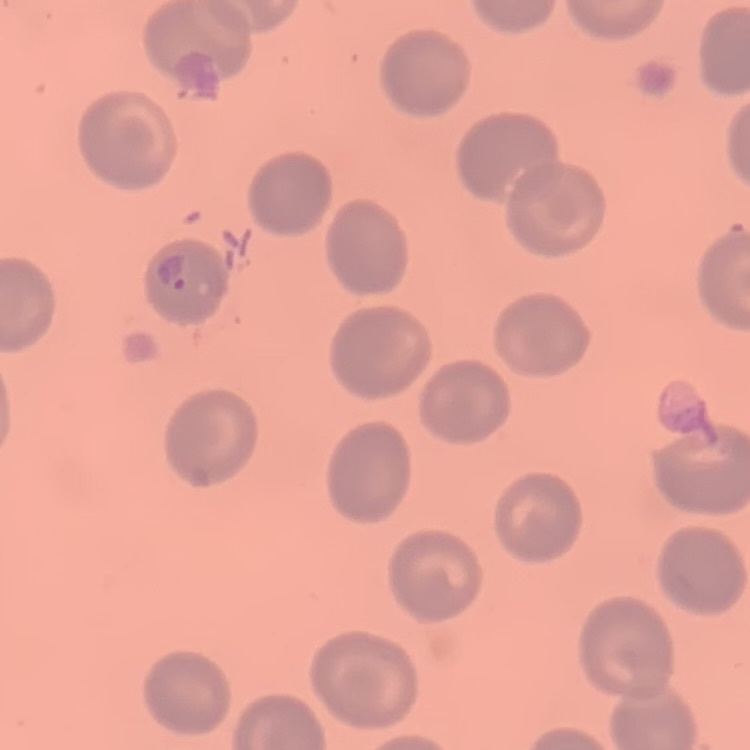

The erythrocytes exhibit no rouleaux formation. Square crop of a larger photomicrograph. Thin blood smear. Stained with either Field's or Giemsa.